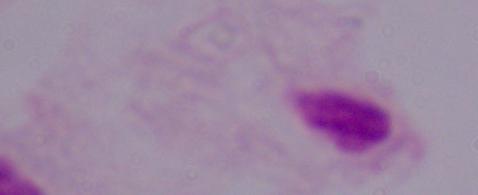 1000x magnification. Micrograph. A trichomonad is shown.